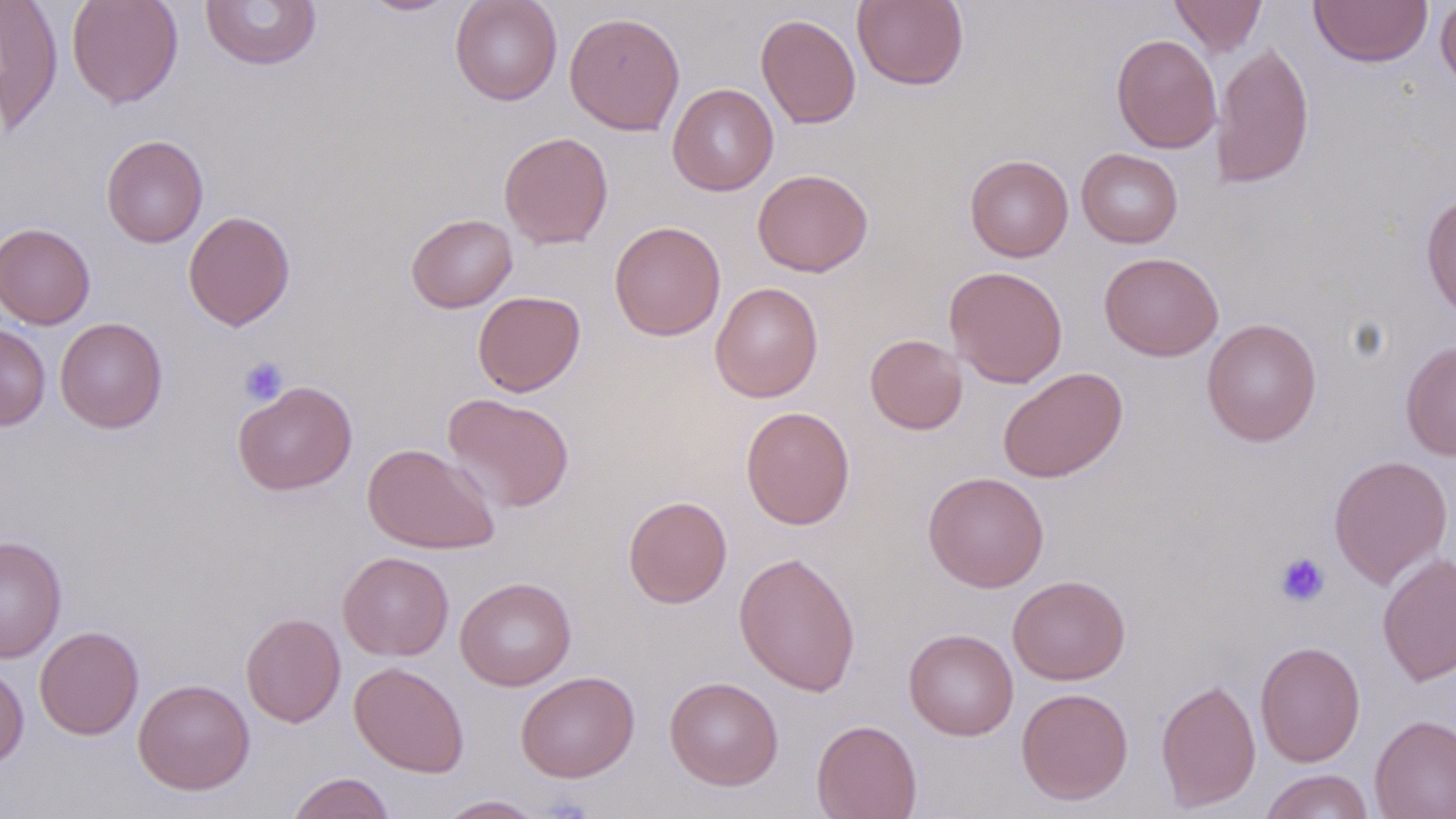
Summary:
  - Coordinate format: approximate bounding boxes as named x1/y1/x2/y2 corners in pixels
  - Uninfected red blood cell locations: (x1=0, y1=0, x2=64, y2=134), (x1=66, y1=0, x2=184, y2=109), (x1=357, y1=0, x2=463, y2=16), (x1=449, y1=0, x2=563, y2=105), (x1=852, y1=0, x2=968, y2=89), (x1=1169, y1=0, x2=1267, y2=57), (x1=1309, y1=0, x2=1433, y2=67), (x1=200, y1=1, x2=323, y2=71), (x1=1435, y1=1, x2=1456, y2=94), (x1=565, y1=11, x2=685, y2=136), (x1=756, y1=14, x2=861, y2=129), (x1=1111, y1=33, x2=1222, y2=153), (x1=1210, y1=41, x2=1314, y2=189), (x1=667, y1=84, x2=779, y2=196), (x1=498, y1=131, x2=614, y2=249), (x1=101, y1=134, x2=209, y2=248), (x1=1076, y1=148, x2=1183, y2=248), (x1=964, y1=154, x2=1073, y2=262), (x1=752, y1=169, x2=873, y2=277), (x1=1420, y1=191, x2=1456, y2=322), (x1=183, y1=210, x2=295, y2=331), (x1=406, y1=213, x2=518, y2=313), (x1=0, y1=222, x2=96, y2=329), (x1=609, y1=222, x2=726, y2=341), (x1=1099, y1=252, x2=1223, y2=361), (x1=943, y1=266, x2=1068, y2=388), (x1=710, y1=282, x2=823, y2=402), (x1=472, y1=290, x2=585, y2=396), (x1=55, y1=316, x2=168, y2=433), (x1=1201, y1=318, x2=1322, y2=446), (x1=0, y1=322, x2=51, y2=431), (x1=865, y1=334, x2=968, y2=434), (x1=1400, y1=339, x2=1456, y2=461), (x1=997, y1=366, x2=1128, y2=483), (x1=233, y1=380, x2=357, y2=496), (x1=441, y1=393, x2=575, y2=513), (x1=740, y1=406, x2=855, y2=529), (x1=362, y1=443, x2=499, y2=554), (x1=1328, y1=454, x2=1453, y2=589), (x1=923, y1=471, x2=1049, y2=592), (x1=623, y1=495, x2=732, y2=608), (x1=0, y1=534, x2=67, y2=663), (x1=733, y1=550, x2=861, y2=696), (x1=337, y1=551, x2=454, y2=661), (x1=1376, y1=551, x2=1456, y2=687), (x1=1007, y1=575, x2=1131, y2=685), (x1=455, y1=576, x2=576, y2=690), (x1=241, y1=612, x2=346, y2=727), (x1=35, y1=625, x2=144, y2=740), (x1=904, y1=629, x2=1018, y2=740), (x1=1254, y1=641, x2=1366, y2=766), (x1=349, y1=661, x2=469, y2=777), (x1=0, y1=663, x2=29, y2=769), (x1=515, y1=670, x2=640, y2=783), (x1=664, y1=676, x2=784, y2=790), (x1=133, y1=678, x2=255, y2=795), (x1=1155, y1=678, x2=1261, y2=812), (x1=1016, y1=687, x2=1134, y2=805), (x1=1369, y1=714, x2=1456, y2=819), (x1=811, y1=719, x2=922, y2=818), (x1=1259, y1=769, x2=1374, y2=819), (x1=286, y1=772, x2=396, y2=819), (x1=435, y1=795, x2=548, y2=818)
  - Platelet locations: (x1=238, y1=356, x2=289, y2=406), (x1=1275, y1=552, x2=1330, y2=607)
  - Slide-level diagnosis: no evidence of blood parasites
  - Stain: May-Grünwald-Giemsa
  - Field of view: one of a larger specimen
  - Modality: optical microscopy
  - Magnification: 1000x
  - Image size: 1456×819 pixels
  - Preparation: thin blood film